Describe the morphology of the erythrocytes.
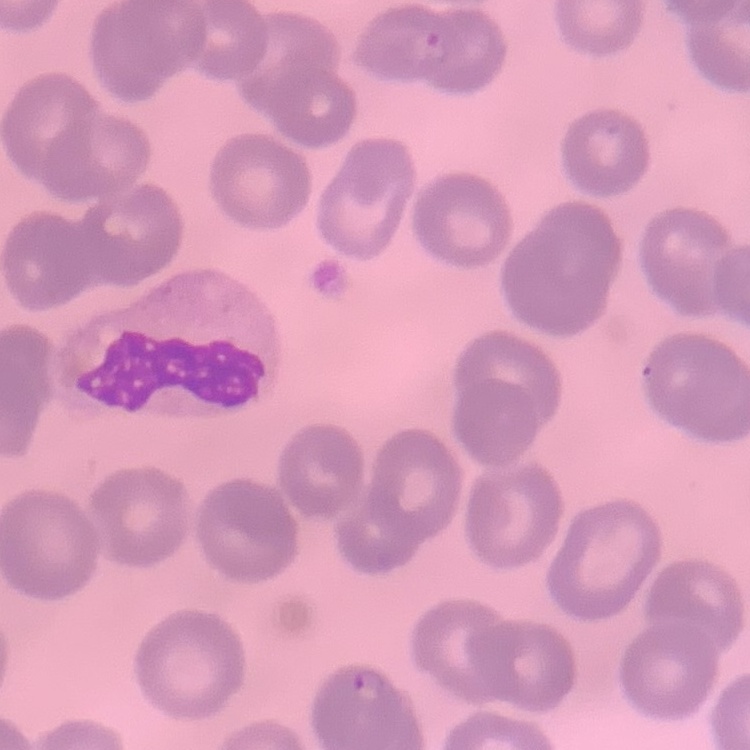
No rouleaux formation.

Square crop of a larger photomicrograph. Stained with either Field's or Giemsa. Thin peripheral smear.